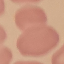
Summary:
  - Malaria status: uninfected
  - Stain: Giemsa
  - Image type: cell patch, automatically extracted from a larger field of view and resized to 64 × 64 pixels
  - Capture: smartphone camera at the microscope eyepiece
  - Preparation: thin blood smear